Classify this cell by malaria status.
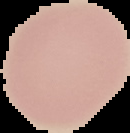

Uninfected.

image_size: 130×133 pixels
preparation: thin blood smear
image_type: segmented cell region with the area outside set to black